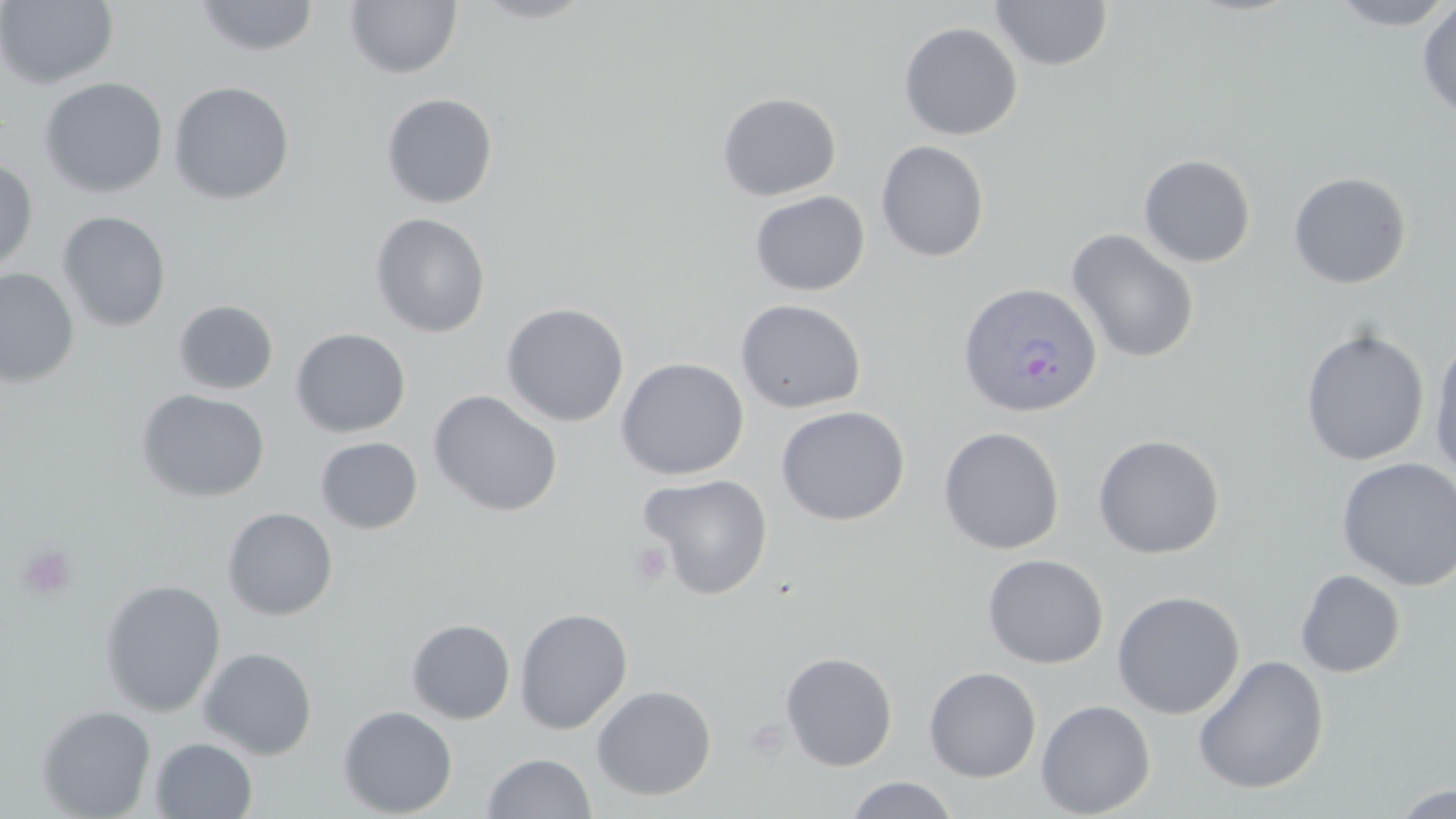

slide-level diagnosis = Plasmodium ovale
modality = light microscopy
Plasmodium ovale-infected red blood cell locations = approximate bounding boxes as (x1, y1, x2, y2) in pixels: (959, 281, 1102, 418)
preparation = thin blood film
field of view = single
platelet locations = approximate bounding boxes as (x1, y1, x2, y2) in pixels: (630, 542, 672, 586), (16, 544, 76, 600), (745, 717, 789, 759)
uninfected red blood cell locations = approximate bounding boxes as (x1, y1, x2, y2) in pixels: (0, 0, 119, 89), (193, 0, 320, 57), (470, 0, 598, 23), (990, 0, 1113, 71), (1328, 0, 1455, 30), (344, 1, 463, 79), (1416, 2, 1456, 118), (898, 22, 1023, 140), (38, 77, 169, 198), (168, 81, 295, 205), (717, 92, 842, 201), (381, 93, 499, 209), (875, 140, 989, 262), (1137, 154, 1257, 267), (0, 158, 38, 275), (1287, 171, 1412, 289), (749, 190, 870, 296), (57, 211, 171, 333), (370, 212, 491, 338), (1065, 229, 1200, 363), (0, 268, 79, 388), (734, 298, 867, 413), (173, 300, 279, 395), (500, 302, 630, 427), (290, 328, 411, 437), (1299, 328, 1430, 467), (1428, 336, 1456, 478), (615, 357, 749, 481), (135, 388, 270, 503), (426, 390, 563, 517), (775, 405, 911, 526), (938, 426, 1065, 555), (1092, 434, 1225, 559), (315, 436, 423, 534), (1336, 457, 1456, 591), (637, 473, 774, 600), (221, 507, 338, 620), (982, 553, 1109, 668), (1295, 569, 1406, 678), (98, 579, 227, 717), (1111, 590, 1245, 719), (514, 607, 633, 734), (406, 618, 515, 724), (197, 646, 318, 760), (780, 651, 898, 771), (1192, 654, 1330, 795), (923, 666, 1041, 782), (591, 684, 717, 801), (1035, 699, 1156, 818), (35, 705, 157, 819), (337, 705, 458, 817), (149, 737, 258, 818), (481, 752, 597, 818), (844, 776, 961, 818), (1389, 784, 1456, 819)
image size = 1456×819 pixels
magnification = 1000x
stain = May-Grünwald-Giemsa